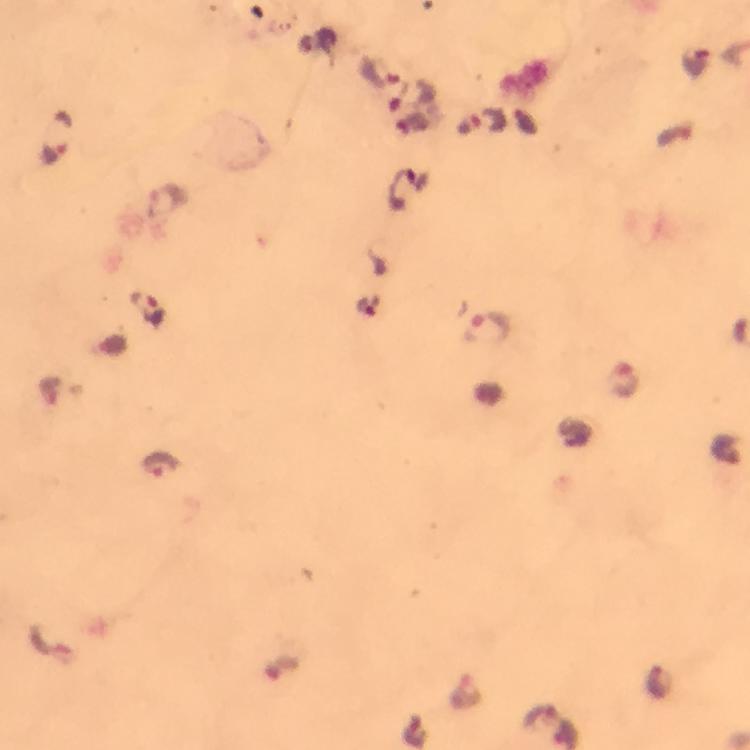
Approximate centers as (x, y) in pixels.
Summary:
  - Plasmodium parasite locations: (381, 73), (413, 99), (491, 123), (57, 138), (168, 202), (147, 308), (489, 329), (625, 380), (726, 449), (159, 465), (660, 683), (464, 691)
  - Image size: 750×750 pixels
  - Capture: smartphone camera through the microscope
  - Magnification: 100x
  - Context: from a diagnostic examination for malaria
  - Stain: Giemsa
  - Immersion oil: used
  - Cropped from: a single field of view
  - Preparation: thick smear